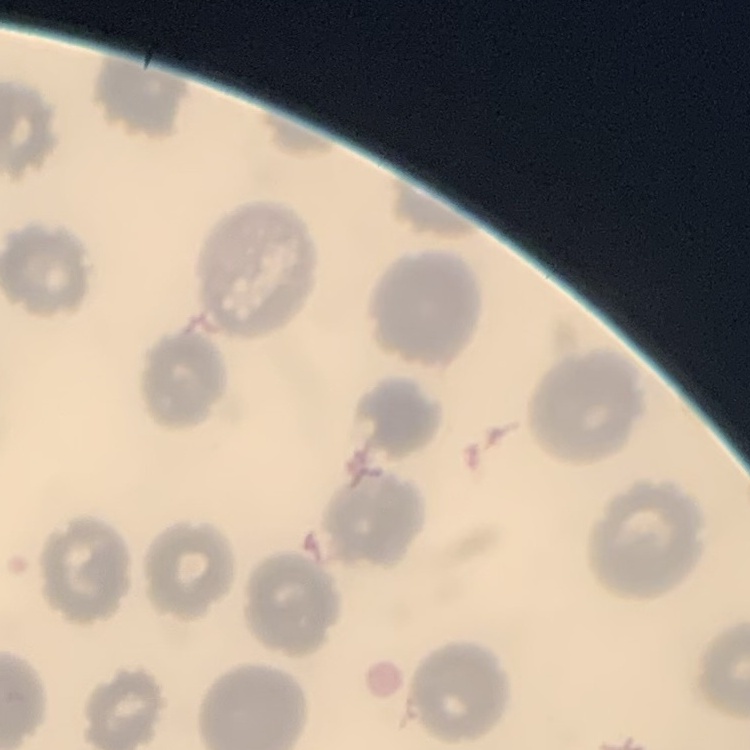
erythrocyte morphology = no rouleaux formation
stain = Field's or Giemsa
image type = one tile cut from a larger photomicrograph
preparation = thin blood smear